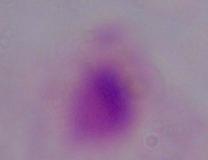

modality = micrograph
magnification = 1000x
identification = trichomonad